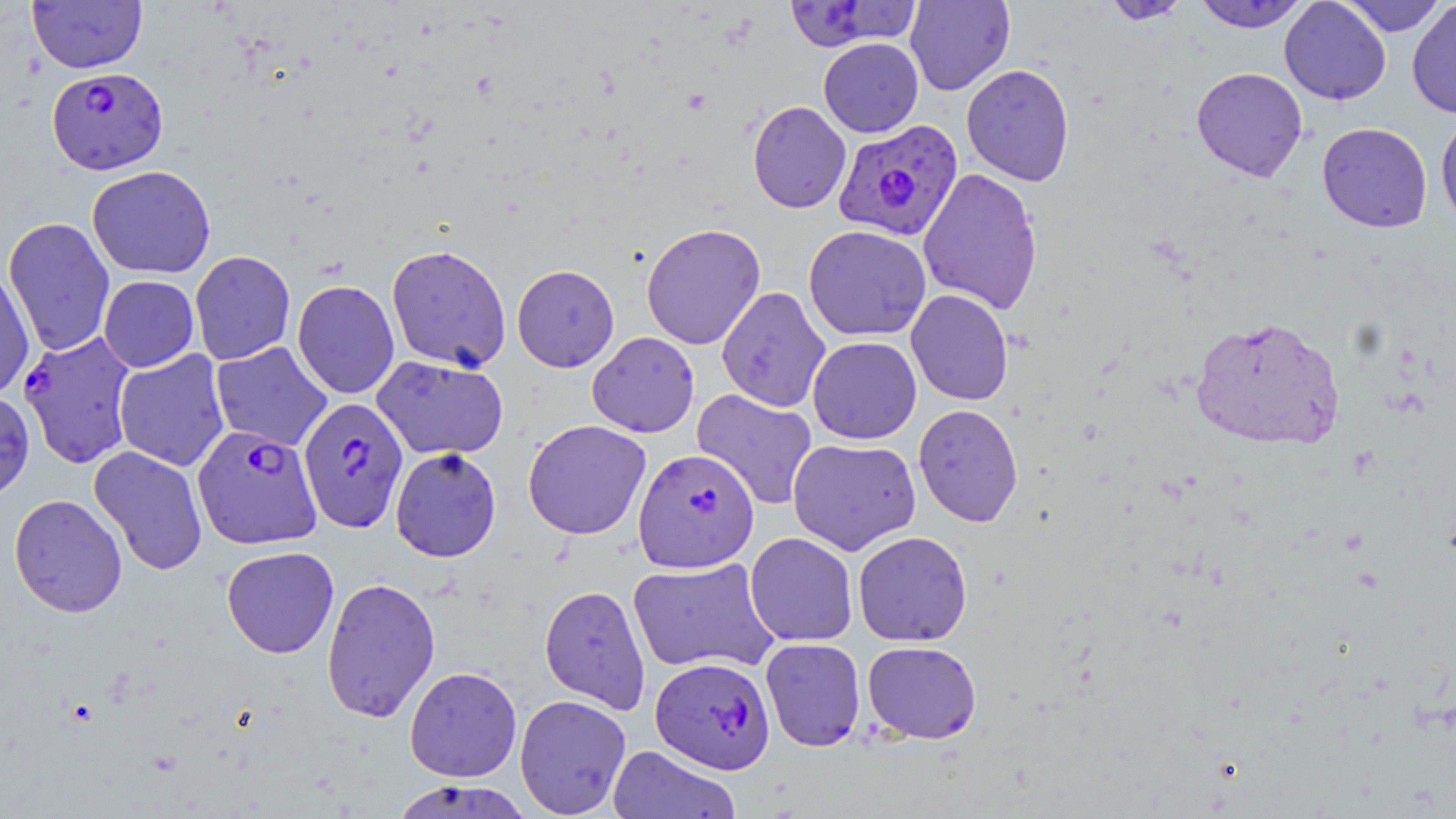

slide-level diagnosis = Plasmodium falciparum
field of view = single
uninfected red blood cell locations = approximate bounding boxes as [x1, y1, x2, y2] in pixels: [27, 0, 147, 74], [905, 0, 1015, 95], [1279, 0, 1391, 105], [1338, 0, 1449, 36], [783, 1, 921, 52], [1099, 1, 1195, 25], [1192, 1, 1311, 32], [1407, 2, 1456, 119], [818, 38, 923, 137], [961, 64, 1075, 186], [1191, 67, 1308, 181], [748, 101, 851, 214], [1435, 115, 1456, 231], [1317, 122, 1433, 233], [87, 165, 216, 279], [918, 168, 1043, 315], [3, 216, 115, 357], [641, 222, 766, 350], [804, 225, 931, 341], [387, 244, 512, 372], [190, 250, 296, 365], [512, 264, 620, 371], [0, 266, 35, 400], [99, 275, 199, 372], [292, 279, 399, 399], [717, 286, 831, 412], [906, 289, 1014, 405], [1189, 314, 1345, 451], [587, 331, 700, 437], [808, 336, 921, 444], [211, 341, 332, 451], [114, 350, 230, 471], [372, 354, 508, 460], [691, 388, 819, 510], [0, 390, 35, 503], [913, 404, 1023, 527], [523, 419, 652, 540], [788, 437, 921, 555], [89, 445, 208, 576], [390, 447, 502, 562], [8, 494, 127, 617], [852, 530, 972, 646], [745, 532, 858, 646], [221, 546, 339, 658], [627, 557, 780, 674], [321, 576, 440, 722], [539, 585, 651, 713], [760, 638, 866, 752], [862, 640, 982, 744], [404, 666, 522, 782], [514, 694, 632, 817], [607, 744, 741, 819], [389, 779, 534, 819]
magnification = 1000x
stain = May-Grünwald-Giemsa
image size = 1456×819 pixels
Plasmodium falciparum-infected red blood cell locations = approximate bounding boxes as [x1, y1, x2, y2] in pixels: [46, 66, 168, 175], [833, 120, 963, 242], [18, 331, 138, 469], [297, 397, 409, 533], [192, 425, 322, 549], [633, 448, 760, 574], [651, 656, 776, 774]
preparation = thin blood film
modality = optical microscopy